State which parasite is depicted.
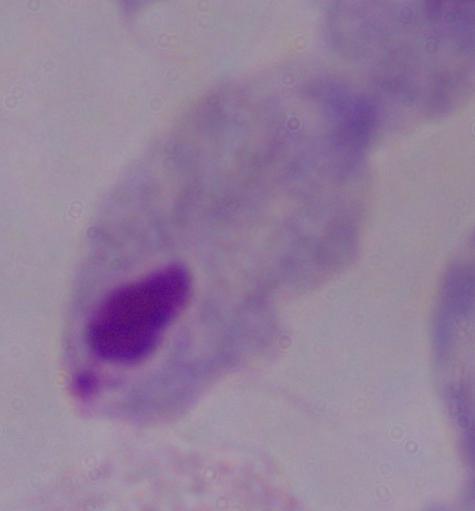
This is a trichomonad.

Photomicrograph. 1000x magnification.